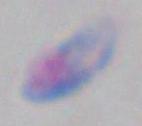
1000x magnification. Toxoplasma gondii is shown. Photomicrograph.